Identify the blood parasite species.
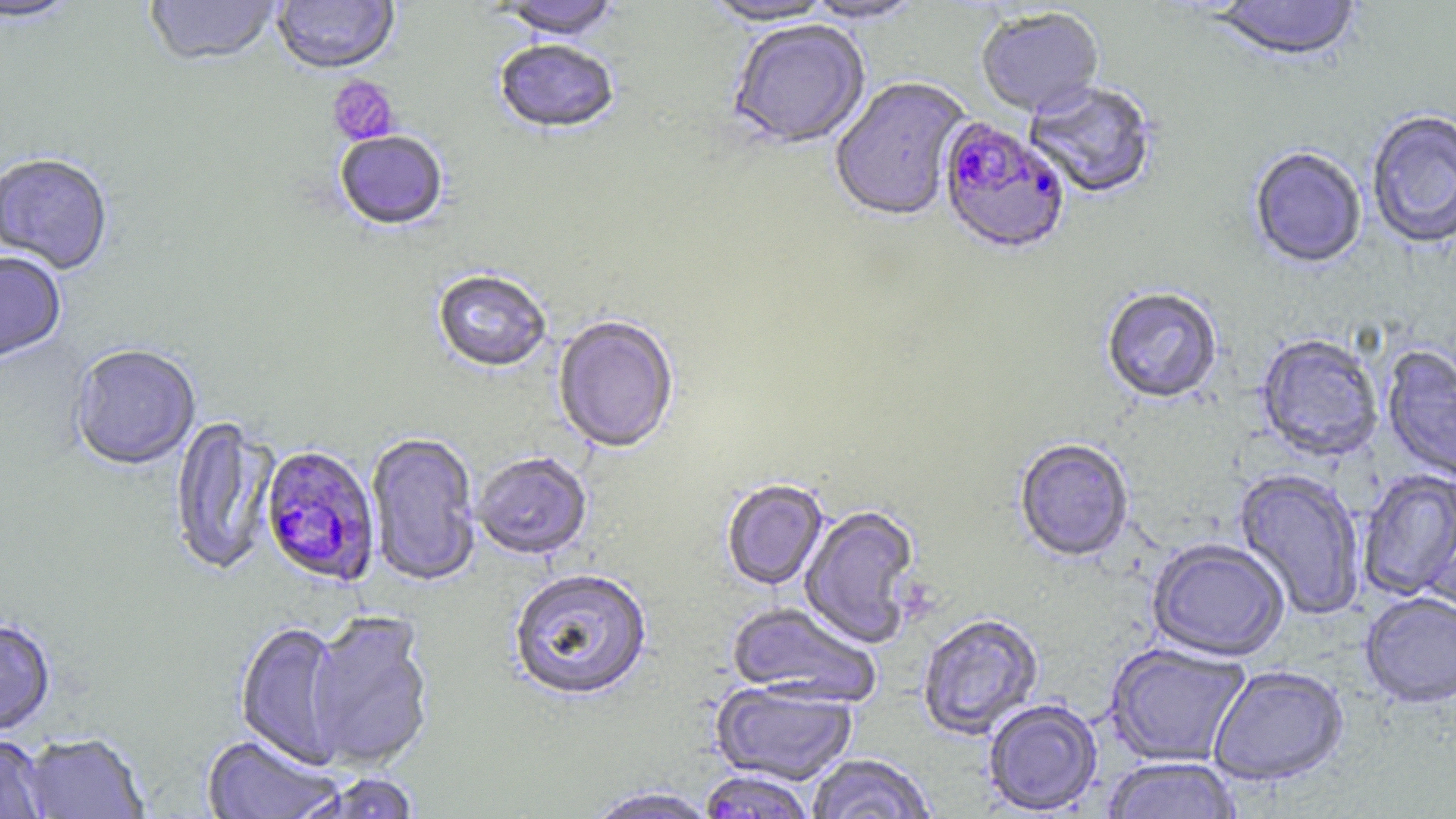

Plasmodium falciparum.

Summary:
  - Coordinate format: approximate bounding boxes as named x1/y1/x2/y2 corners in pixels
  - Platelet locations: (x1=327, y1=75, x2=399, y2=146)
  - Uninfected red blood cell locations: (x1=144, y1=0, x2=281, y2=69), (x1=494, y1=0, x2=621, y2=43), (x1=699, y1=0, x2=840, y2=28), (x1=800, y1=0, x2=926, y2=26), (x1=1210, y1=0, x2=1361, y2=65), (x1=0, y1=1, x2=81, y2=27), (x1=271, y1=1, x2=400, y2=77), (x1=976, y1=9, x2=1104, y2=119), (x1=728, y1=21, x2=871, y2=152), (x1=493, y1=42, x2=620, y2=137), (x1=829, y1=77, x2=973, y2=224), (x1=1023, y1=82, x2=1158, y2=200), (x1=1366, y1=111, x2=1456, y2=251), (x1=335, y1=133, x2=448, y2=233), (x1=1248, y1=148, x2=1366, y2=271), (x1=0, y1=155, x2=113, y2=276), (x1=0, y1=253, x2=66, y2=363), (x1=432, y1=271, x2=551, y2=374), (x1=1101, y1=289, x2=1222, y2=407), (x1=553, y1=316, x2=679, y2=455), (x1=1255, y1=335, x2=1384, y2=463), (x1=70, y1=346, x2=201, y2=472), (x1=1381, y1=346, x2=1456, y2=484), (x1=169, y1=417, x2=281, y2=579), (x1=367, y1=433, x2=480, y2=587), (x1=1014, y1=440, x2=1134, y2=564), (x1=472, y1=453, x2=593, y2=561), (x1=1232, y1=468, x2=1364, y2=621), (x1=1358, y1=470, x2=1456, y2=602), (x1=721, y1=480, x2=829, y2=591), (x1=800, y1=505, x2=921, y2=649), (x1=1147, y1=540, x2=1289, y2=663), (x1=508, y1=569, x2=653, y2=703), (x1=1360, y1=594, x2=1456, y2=710), (x1=727, y1=602, x2=882, y2=707), (x1=304, y1=611, x2=435, y2=771), (x1=917, y1=614, x2=1044, y2=740), (x1=0, y1=619, x2=56, y2=736), (x1=235, y1=621, x2=346, y2=767), (x1=1104, y1=642, x2=1251, y2=768), (x1=1209, y1=667, x2=1349, y2=788), (x1=711, y1=681, x2=858, y2=787), (x1=983, y1=700, x2=1103, y2=815), (x1=21, y1=734, x2=149, y2=818), (x1=200, y1=734, x2=344, y2=818), (x1=0, y1=735, x2=50, y2=819), (x1=806, y1=755, x2=937, y2=819), (x1=1102, y1=758, x2=1243, y2=819), (x1=699, y1=770, x2=815, y2=819), (x1=296, y1=773, x2=422, y2=819), (x1=583, y1=786, x2=720, y2=819)
  - Plasmodium falciparum-infected red blood cell locations: (x1=938, y1=118, x2=1070, y2=258), (x1=260, y1=446, x2=380, y2=587)
  - Field of view: single
  - Magnification: 1000x
  - Preparation: thin blood film
  - Modality: light microscopy
  - Stain: May-Grünwald-Giemsa
  - Image size: 1456×819 pixels